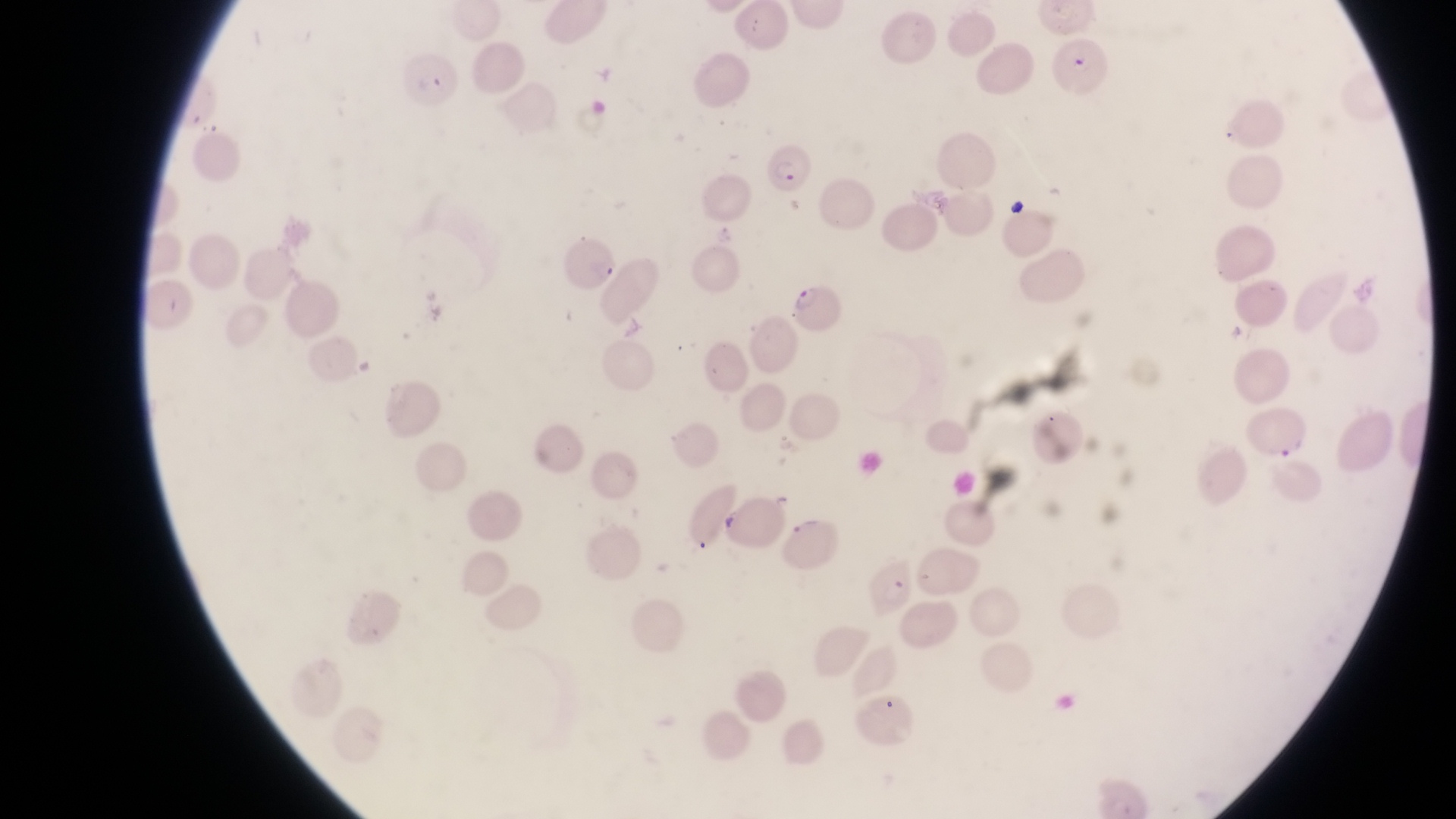
country: Uganda
field_of_view: single
preparation: thin blood smear
capture: smartphone photograph through the eyepiece of an Olympus CX-23 microscope
parasitised_red_blood_cell_locations: 'approximate bounding boxes as left top right bottom in pixels: 1049 34 1113 105; 403 59 466 109; 763 146 818 195; 563 237 621 295; 792 281 851 334'
image_size: 1456×819 pixels
magnification: 1000x